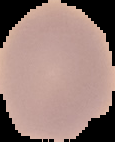

Image is 115×142 pixels. From a thin blood film. Malaria status: uninfected. Segmented cell region on a black background.